Give the extent of all Plasmodium falciparum-infected red blood cells.
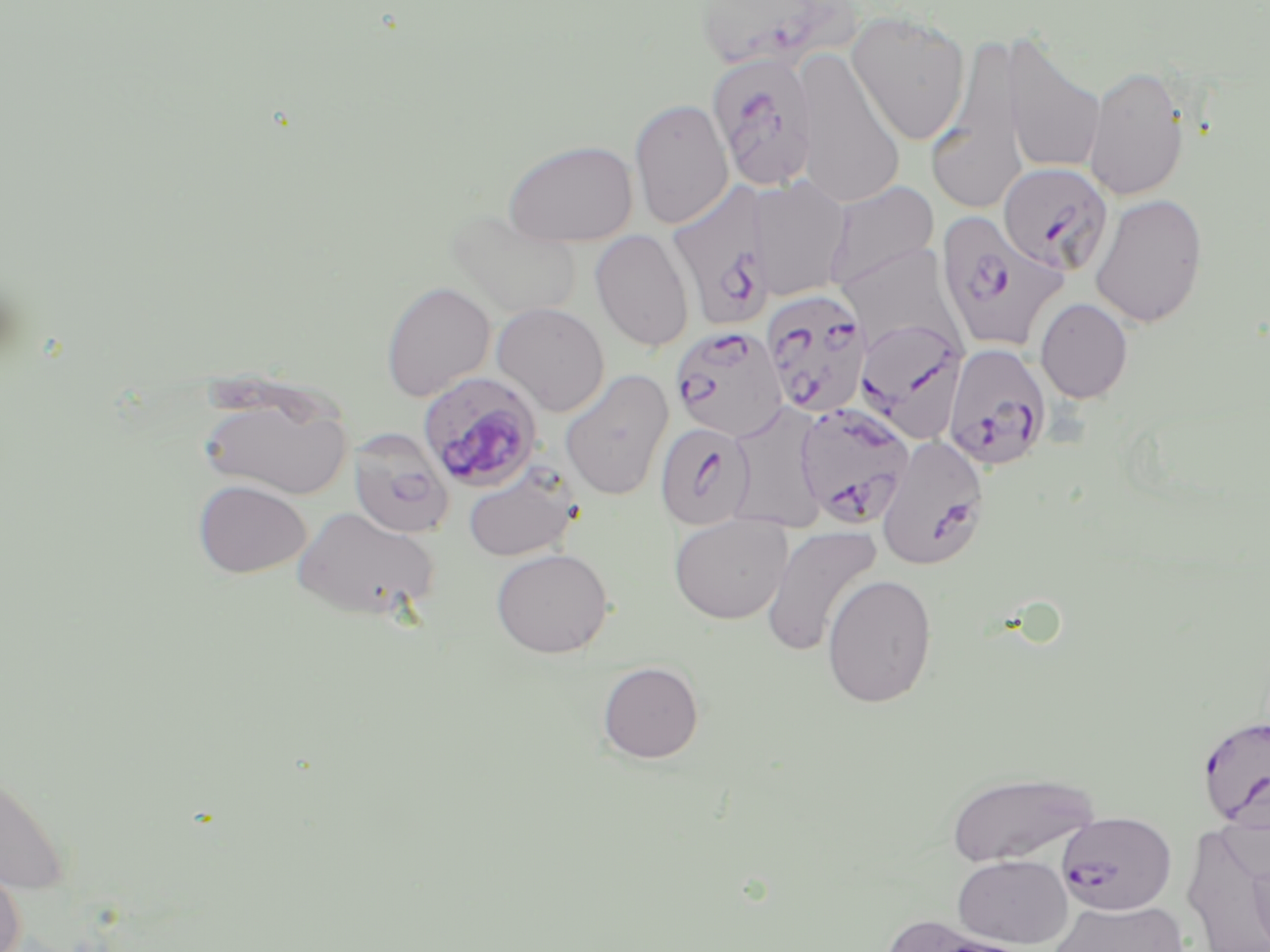
Approximate bounding boxes as (x1,y1)-(x2,y2) corner pairs in pixels.
Plasmodium falciparum-infected red blood cells: (693,0)-(857,74), (713,56)-(813,189), (998,162)-(1114,276), (667,186)-(777,334), (936,211)-(1068,355), (762,289)-(873,419), (856,317)-(969,441), (669,324)-(790,442), (942,343)-(1052,471), (425,374)-(540,486), (793,403)-(916,530), (654,422)-(756,529), (348,427)-(454,539), (877,434)-(989,571), (1196,714)-(1270,831), (1057,811)-(1177,916).

Summary:
  - Uninfected red blood cell locations: (847,11)-(971,145), (999,33)-(1106,174), (929,34)-(1032,213), (792,49)-(905,208), (1083,64)-(1191,202), (629,97)-(733,230), (502,139)-(639,246), (749,176)-(852,301), (823,181)-(939,292), (1089,193)-(1208,329), (446,210)-(584,320), (590,228)-(694,352), (837,241)-(963,354), (381,282)-(495,401), (1035,298)-(1133,403), (491,302)-(610,416), (559,369)-(675,501), (197,386)-(353,501), (725,404)-(829,533), (462,462)-(582,562), (193,480)-(311,577), (293,505)-(441,622), (669,513)-(793,625), (761,524)-(883,657), (490,548)-(614,658), (822,573)-(938,708), (597,661)-(704,763), (0,763)-(71,898), (946,770)-(1100,866), (953,854)-(1072,947), (1248,855)-(1270,950), (0,861)-(26,952), (1050,899)-(1189,952)
  - Slide-level diagnosis: Plasmodium falciparum
  - Preparation: thin blood film
  - Image size: 1270×952 pixels
  - Stain: May-Grünwald-Giemsa
  - Modality: light microscopy
  - Magnification: 1000x
  - Field of view: single